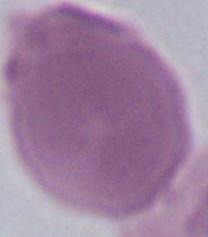

Summary:
  - Modality: photomicrograph
  - Identification: red blood cell
  - Magnification: 1000x